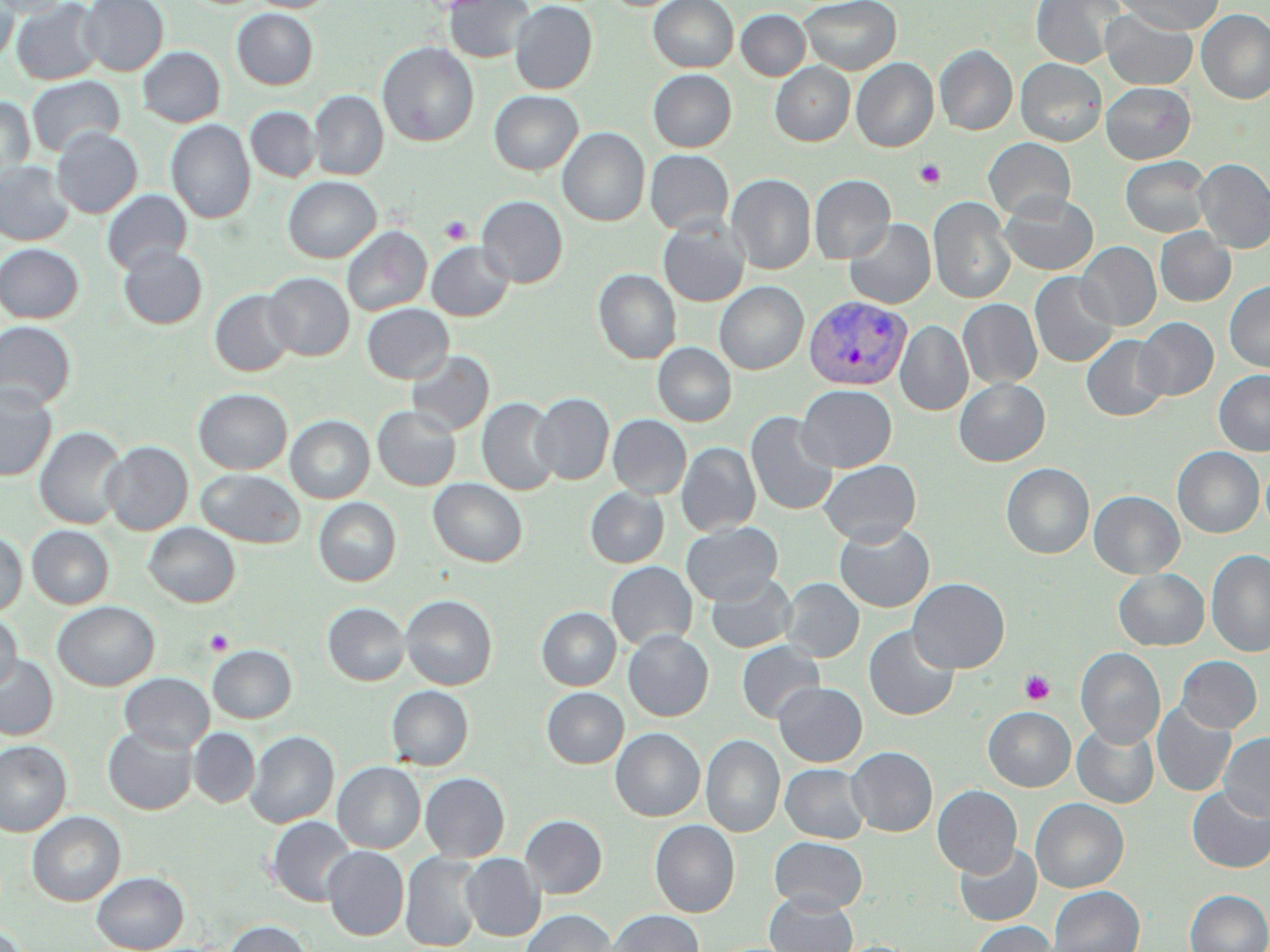
Approximate bounding boxes as (x1,y1)-(x2,y2) corner pairs in pixels. Platelet locations: (914,159)-(946,188), (439,216)-(471,245), (204,629)-(234,656), (1019,670)-(1055,706). Plasmodium vivax-infected red blood cell locations: (804,295)-(912,390). Uninfected red blood cell locations: (1,0)-(70,18), (79,0)-(168,75), (248,0)-(335,12), (444,0)-(534,63), (648,0)-(738,72), (800,0)-(901,74), (1029,0)-(1126,68), (1116,0)-(1225,35), (0,1)-(19,64), (12,1)-(104,85), (510,1)-(597,94), (233,9)-(318,89), (736,9)-(811,80), (1196,9)-(1270,104), (1101,10)-(1198,89), (377,42)-(479,147), (935,45)-(1018,135), (138,46)-(225,127), (852,58)-(938,152), (1016,58)-(1107,146), (771,63)-(855,145), (648,69)-(736,152), (26,75)-(124,157), (1101,82)-(1195,164), (1112,83)-(1201,238), (489,90)-(583,175), (309,91)-(388,179), (0,97)-(35,182), (246,107)-(321,182), (166,120)-(255,223), (52,128)-(142,218), (558,128)-(649,226), (984,138)-(1076,220), (645,150)-(734,235), (1120,156)-(1212,237), (1195,158)-(1270,253), (0,161)-(73,246), (727,174)-(816,274), (809,174)-(895,263), (283,176)-(381,263), (102,189)-(192,274), (999,192)-(1098,275), (477,196)-(568,287), (928,197)-(1016,304), (658,218)-(749,307), (844,218)-(936,309), (342,226)-(432,316), (1154,228)-(1236,306), (426,241)-(514,321), (1076,241)-(1161,330), (0,243)-(84,323), (118,245)-(207,329), (593,269)-(681,364), (1029,271)-(1119,367), (264,272)-(354,361), (1224,280)-(1270,372), (714,281)-(808,374), (209,289)-(297,377), (958,299)-(1042,389), (362,303)-(453,383), (1134,317)-(1218,400), (896,320)-(973,415), (0,321)-(76,410), (1081,334)-(1170,421), (652,343)-(737,426), (407,350)-(494,435), (1214,370)-(1270,456), (954,378)-(1050,466), (796,385)-(897,472), (0,386)-(57,481), (193,388)-(292,474), (531,392)-(614,485), (477,397)-(561,495), (372,405)-(461,491), (745,411)-(839,515), (608,414)-(691,499), (286,415)-(375,503), (35,426)-(127,529), (102,441)-(193,535), (677,442)-(761,536), (1172,447)-(1264,538), (819,459)-(921,546), (1001,463)-(1094,559), (196,469)-(305,547), (429,478)-(528,567), (585,487)-(669,567), (1089,490)-(1185,578), (313,497)-(401,586), (144,522)-(241,607), (681,522)-(782,605), (834,522)-(934,612), (27,525)-(114,609), (0,531)-(27,616), (1206,549)-(1270,656), (606,561)-(697,650), (1113,569)-(1209,650), (706,573)-(797,653), (780,578)-(864,662), (908,578)-(1010,673), (401,595)-(497,690), (53,601)-(159,691), (322,602)-(410,685), (537,607)-(621,690), (0,613)-(21,691), (863,625)-(959,721), (623,630)-(713,721), (736,641)-(825,723), (208,646)-(296,723), (1075,648)-(1165,748), (0,654)-(58,740), (1176,656)-(1261,733), (119,673)-(214,753), (773,682)-(867,766), (386,686)-(473,770), (542,688)-(628,768), (1152,703)-(1237,798), (983,706)-(1076,791), (1072,721)-(1159,808), (103,726)-(198,815), (189,728)-(260,808), (611,728)-(705,821), (246,730)-(339,828), (1219,732)-(1270,821), (701,735)-(784,837), (0,740)-(72,837), (847,746)-(937,836), (333,761)-(425,853), (781,763)-(870,843), (421,772)-(510,862), (932,785)-(1022,877), (1186,785)-(1270,873), (1030,798)-(1129,892), (27,811)-(125,906), (520,815)-(607,898), (267,816)-(356,906), (650,820)-(739,917), (769,836)-(868,912), (954,843)-(1042,926), (323,846)-(408,940), (400,852)-(485,951), (461,853)-(545,940), (92,871)-(188,952), (1049,886)-(1145,952), (1184,889)-(1270,952), (764,893)-(858,952), (520,909)-(617,952), (608,910)-(704,952), (224,920)-(312,952), (972,920)-(1058,952). Slide-level diagnosis: Plasmodium vivax. May-Grünwald-Giemsa stain. Thin blood smear. Captured at 1000x magnification. One field of a larger specimen. Light microscopy. Image is 1270×952 pixels.